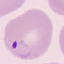

Summary:
  - Malaria status: parasitized
  - Image type: automatically extracted cell patch, resized to 64 × 64 pixels
  - Preparation: thin blood smear
  - Stain: Giemsa
  - Capture: smartphone through the microscope eyepiece